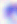

identification = Toxoplasma gondii
magnification = 400x
modality = photomicrograph